Name the parasite shown.
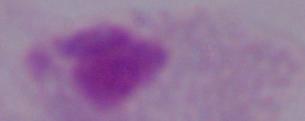

This is a trichomonad.

Micrograph. Captured at 1000x magnification.